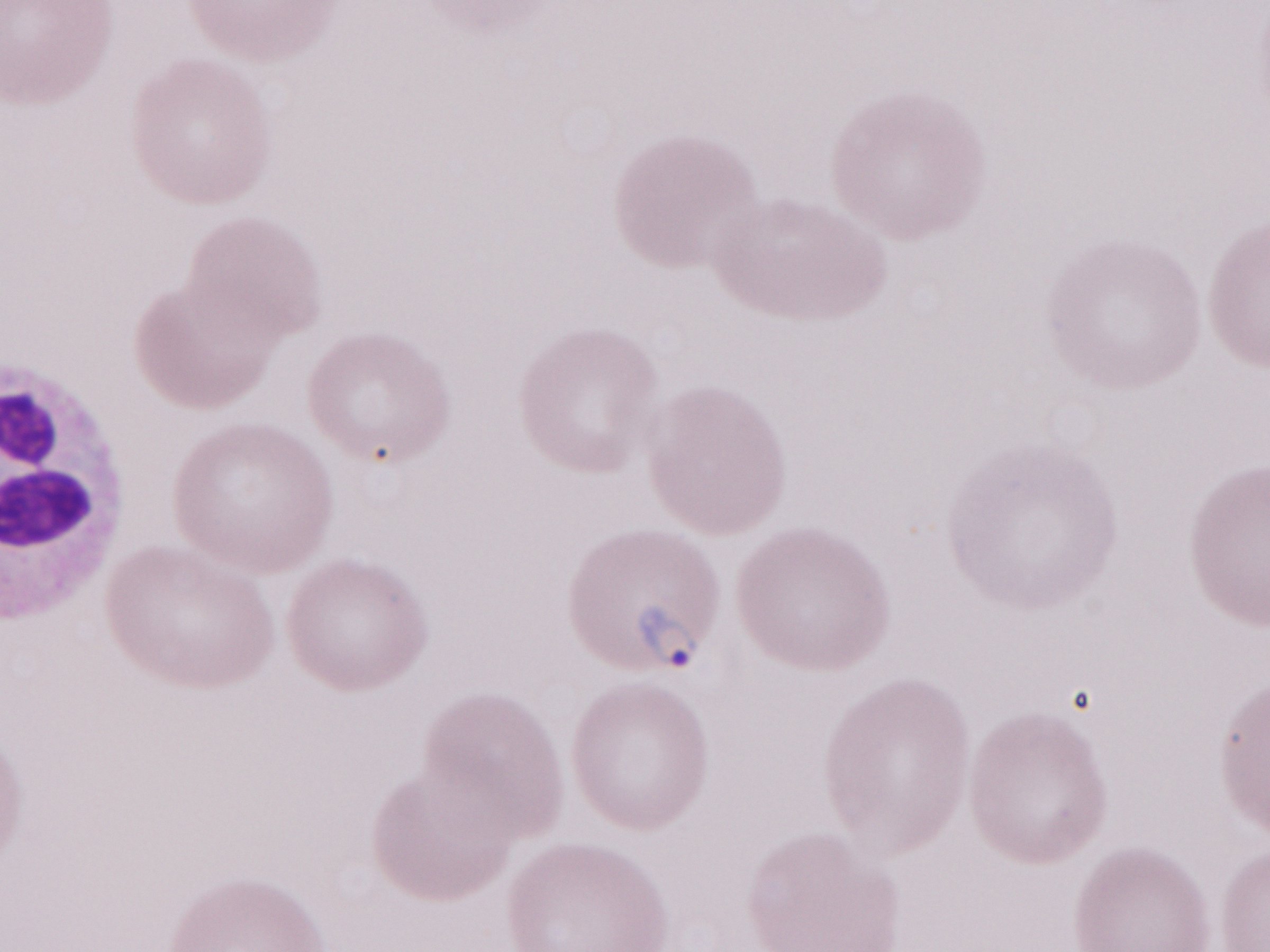 Single field of view. 1,000x magnification. Malaria diagnosis (patient-level): positive. Thin blood smear. Image is 1270×952 pixels. Olympus BX43 microscope and DP73 digital camera. May-Grünwald-Giemsa stain.